Point out each malaria parasite.
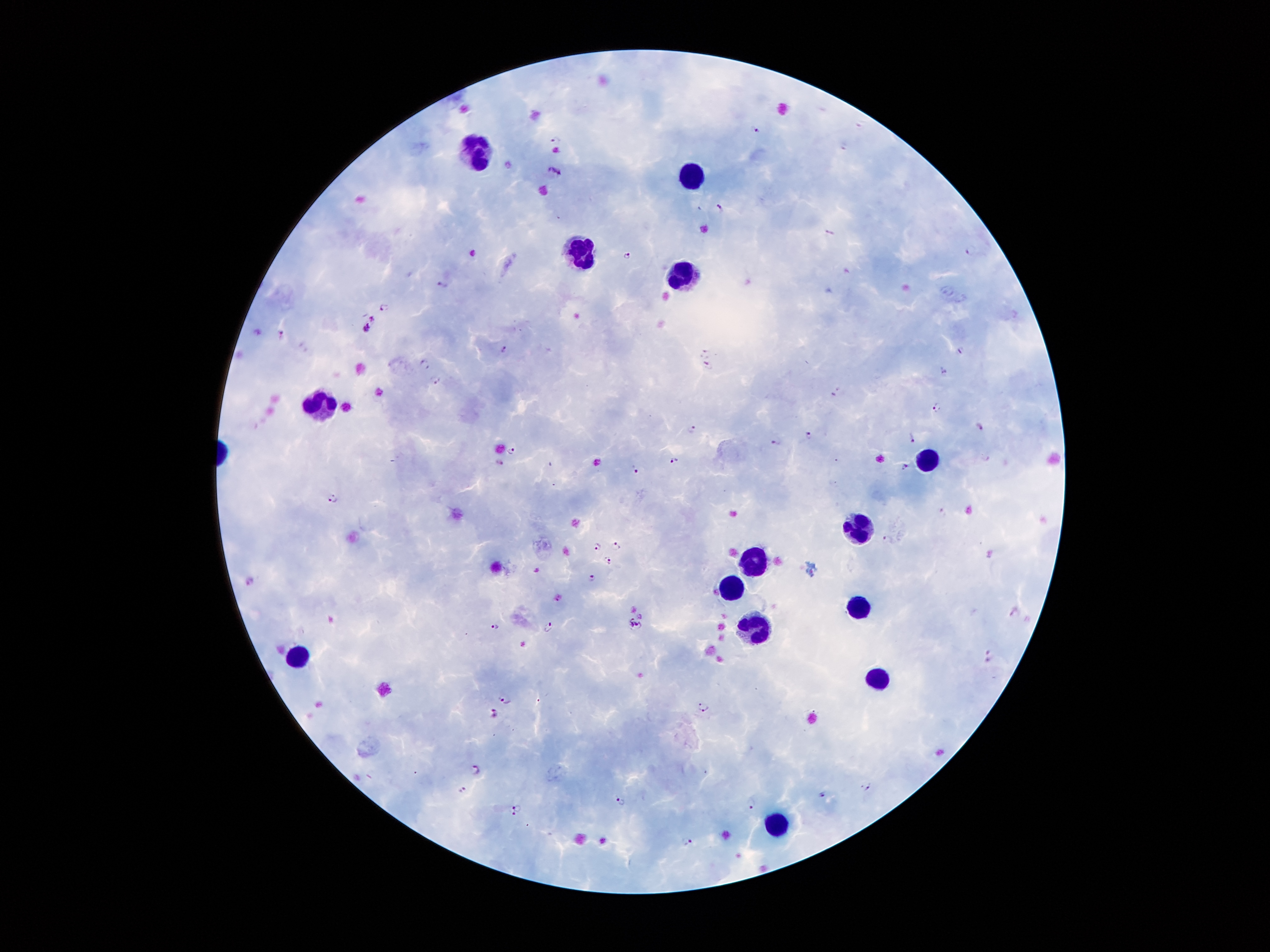
Approximate centers as {x, y} in pixels.
Malaria parasites: {556, 141}, {554, 170}, {720, 208}, {472, 253}, {627, 256}, {444, 286}, {383, 311}, {368, 327}, {281, 334}, {504, 350}, {960, 350}, {704, 353}, {427, 365}, {709, 366}, {944, 372}, {436, 381}, {936, 407}, {979, 426}, {692, 429}, {809, 436}, {912, 438}, {775, 443}, {512, 450}, {675, 461}, {499, 462}, {904, 466}, {635, 469}, {335, 498}, {886, 537}, {615, 546}, {598, 547}, {609, 560}, {538, 570}, {593, 576}, {249, 582}, {1015, 612}, {636, 624}, {496, 626}, {548, 627}, {989, 656}, {505, 700}, {702, 706}, {492, 712}, {478, 770}, {869, 785}, {461, 790}, {821, 794}, {622, 800}, {751, 803}, {518, 807}, {513, 815}, {688, 841}.

Summary:
  - Leukocyte locations: {471, 151}, {694, 173}, {577, 249}, {678, 274}, {324, 404}, {930, 454}, {861, 523}, {750, 562}, {733, 589}, {863, 606}, {762, 628}, {299, 657}, {874, 677}, {778, 824}
  - Stain: Giemsa
  - Capture: smartphone camera through the microscope eyepiece
  - Preparation: thick blood film
  - Magnification: 100x
  - Patient malaria status: infected with Plasmodium falciparum
  - Image size: 1270×952 pixels
  - Field of view: one from this slide